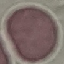
Malaria status: uninfected. Giemsa-stained preparation. Thin smear of blood. Acquired by smartphone through the microscope eyepiece. Automatically extracted cell patch, resized to 64 × 64 pixels.